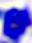 Captured at 400x magnification. A white blood cell is seen. Micrograph.